Identify the parasite.
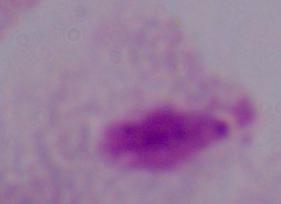
This is a trichomonad.

Summary:
  - Magnification: 1000x
  - Modality: photomicrograph